Classify this cell by malaria status.
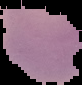
It is uninfected.

Summary:
  - Image size: 82×85 pixels
  - Preparation: thin blood film
  - Image type: cell region segmented out of the field of view; surrounding area masked to black